Point out each malaria parasite.
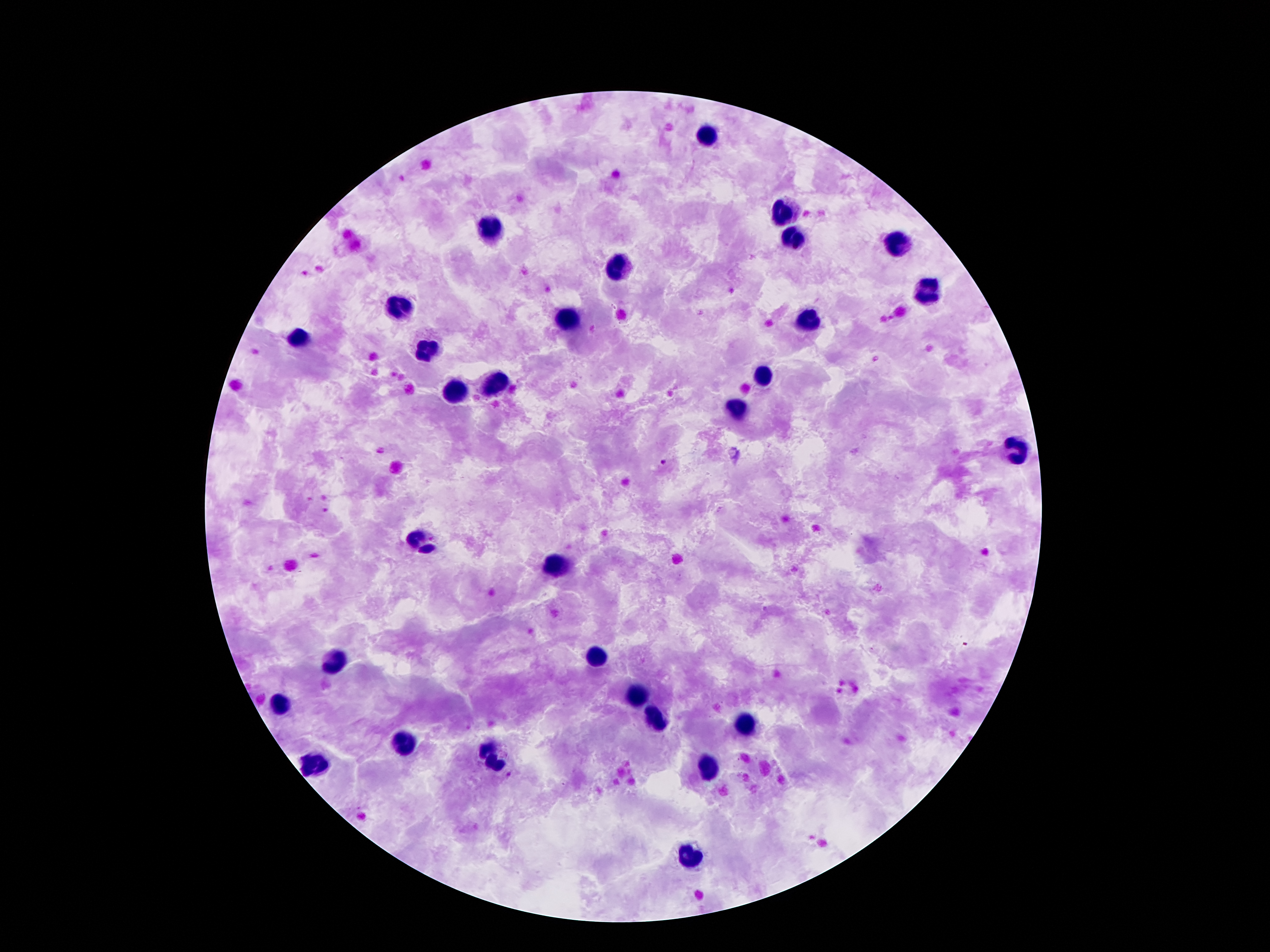
Approximate centers as [x, y] in pixels.
Malaria parasites: [663, 463].

{
  "image_size": "1270×952 pixels",
  "preparation": "thick blood film",
  "capture": "smartphone camera through the microscope eyepiece",
  "magnification": "100x",
  "stain": "Giemsa",
  "leukocyte_locations": "approximate centers as [x, y] in pixels: [707, 134], [783, 214], [491, 230], [796, 239], [898, 242], [615, 269], [926, 288], [399, 307], [567, 317], [810, 320], [302, 338], [424, 347], [764, 376], [491, 386], [458, 391], [735, 407], [1018, 452], [422, 540], [554, 566], [598, 657], [334, 661], [632, 695], [281, 705], [655, 715], [745, 724], [405, 749], [491, 758], [311, 762], [710, 766], [689, 859]",
  "field_of_view": "one from this slide",
  "patient_malaria_status": "positive for Plasmodium falciparum"
}